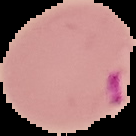
image size = 136×136 pixels
image type = segmented cell region with the area outside set to black
preparation = thin blood smear
malaria status = parasitized